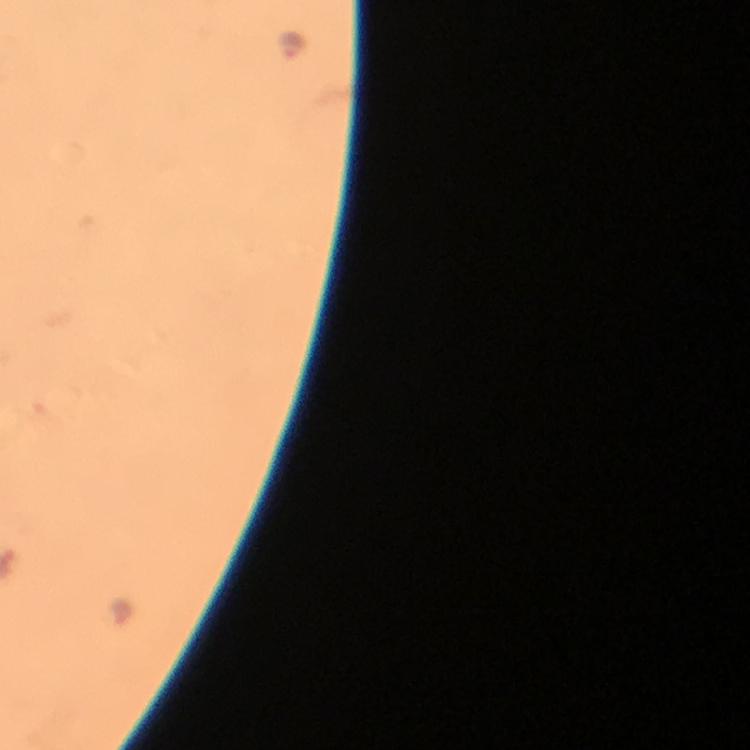

{
  "cropped_from": "one field of view",
  "preparation": "thick smear",
  "immersion_oil": "applied",
  "magnification": "100x",
  "plasmodium_parasite_locations": "approximate object centers, in pixels from the top-left corner: (x=293, y=45), (x=124, y=609)",
  "image_size": "750×750 pixels",
  "context": "from a diagnostic examination for malaria",
  "stain": "Giemsa",
  "capture": "smartphone mounted on the microscope"
}